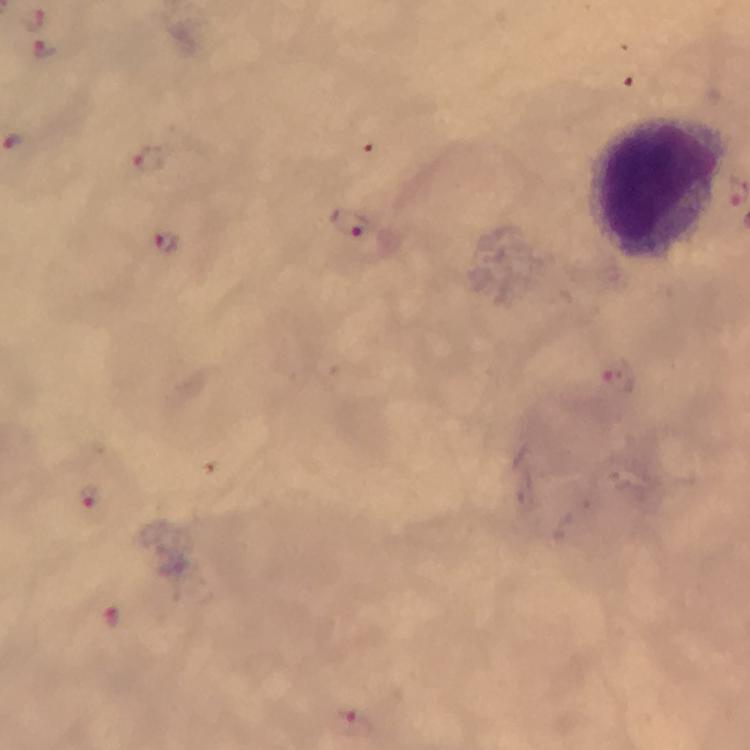
Approximate centers as {x, y} in pixels.
Summary:
  - Plasmodium parasite locations: {32, 17}, {43, 49}, {152, 159}, {352, 228}, {165, 244}, {620, 382}, {89, 500}, {109, 618}, {349, 723}
  - Leukocyte locations: {658, 190}
  - Stain: Giemsa
  - Image size: 750×750 pixels
  - Preparation: thick smear
  - Immersion oil: applied
  - Magnification: 100x
  - Cropped from: a single field of view
  - Capture: smartphone camera through the microscope
  - Context: from a diagnostic examination for malaria